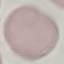 Malaria status: uninfected. Cell patch, automatically extracted from a larger field of view and resized to 64 × 64 pixels. Giemsa-stained preparation. Acquired by smartphone through the microscope eyepiece. Thin smear of blood.